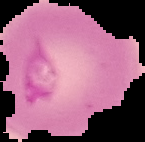
{
  "image_size": "145×142 pixels",
  "result": "Plasmodium parasites detected",
  "image_type": "segmented cell region on a black background",
  "preparation": "thin blood film"
}